Locate platelets.
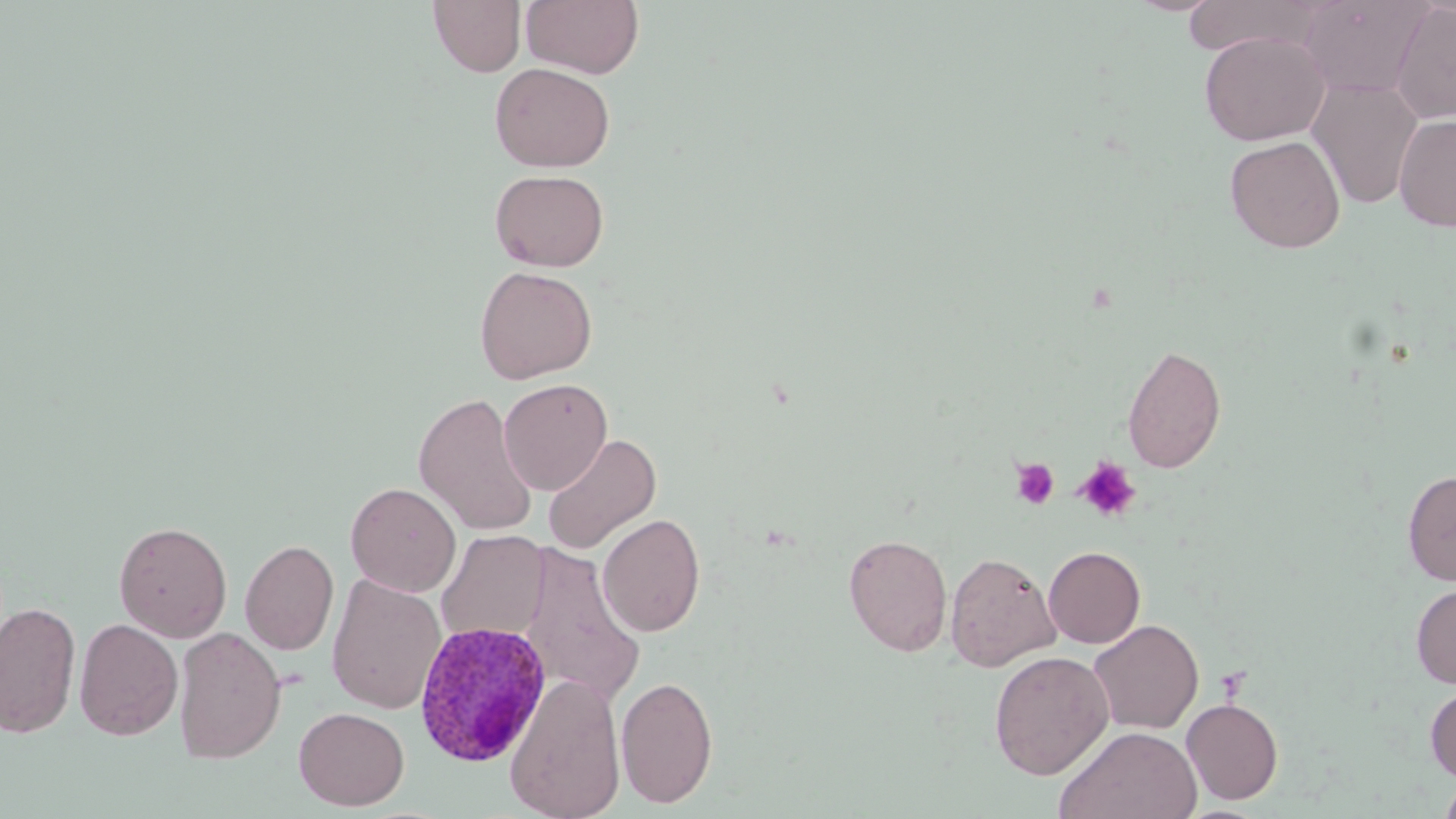

Approximate bounding boxes as named x1/y1/x2/y2 corners in pixels.
Platelets: (x1=1010, y1=457, x2=1059, y2=510), (x1=1074, y1=457, x2=1141, y2=523).

Plasmodium ovale-infected red blood cell locations: (x1=413, y1=621, x2=551, y2=766). Uninfected red blood cell locations: (x1=428, y1=0, x2=526, y2=76), (x1=521, y1=0, x2=644, y2=78), (x1=1182, y1=0, x2=1322, y2=56), (x1=1296, y1=0, x2=1433, y2=97), (x1=1389, y1=2, x2=1456, y2=123), (x1=1199, y1=31, x2=1330, y2=145), (x1=490, y1=62, x2=615, y2=172), (x1=1307, y1=76, x2=1423, y2=210), (x1=1394, y1=114, x2=1456, y2=232), (x1=1224, y1=135, x2=1346, y2=253), (x1=489, y1=168, x2=610, y2=272), (x1=474, y1=265, x2=598, y2=383), (x1=1122, y1=343, x2=1227, y2=474), (x1=498, y1=378, x2=613, y2=495), (x1=413, y1=392, x2=538, y2=536), (x1=541, y1=432, x2=662, y2=554), (x1=1402, y1=469, x2=1456, y2=586), (x1=345, y1=482, x2=461, y2=596), (x1=597, y1=513, x2=706, y2=637), (x1=114, y1=520, x2=232, y2=642), (x1=436, y1=529, x2=549, y2=645), (x1=842, y1=533, x2=953, y2=656), (x1=239, y1=539, x2=339, y2=655), (x1=521, y1=543, x2=646, y2=712), (x1=1043, y1=546, x2=1145, y2=648), (x1=945, y1=552, x2=1061, y2=672), (x1=326, y1=572, x2=446, y2=714), (x1=1411, y1=581, x2=1456, y2=689), (x1=0, y1=601, x2=81, y2=738), (x1=74, y1=618, x2=183, y2=740), (x1=1087, y1=619, x2=1204, y2=734), (x1=173, y1=627, x2=286, y2=765), (x1=989, y1=650, x2=1114, y2=779), (x1=504, y1=672, x2=626, y2=819), (x1=615, y1=674, x2=718, y2=808), (x1=1424, y1=683, x2=1456, y2=783), (x1=1181, y1=698, x2=1283, y2=804), (x1=293, y1=707, x2=409, y2=811), (x1=1055, y1=724, x2=1202, y2=819), (x1=1437, y1=772, x2=1456, y2=819). Slide-level diagnosis: Plasmodium ovale. Single field of view. Light microscopy. Image is 1456×819 pixels. Thin blood film. May-Grünwald-Giemsa-stained preparation. Captured at 1000x magnification.